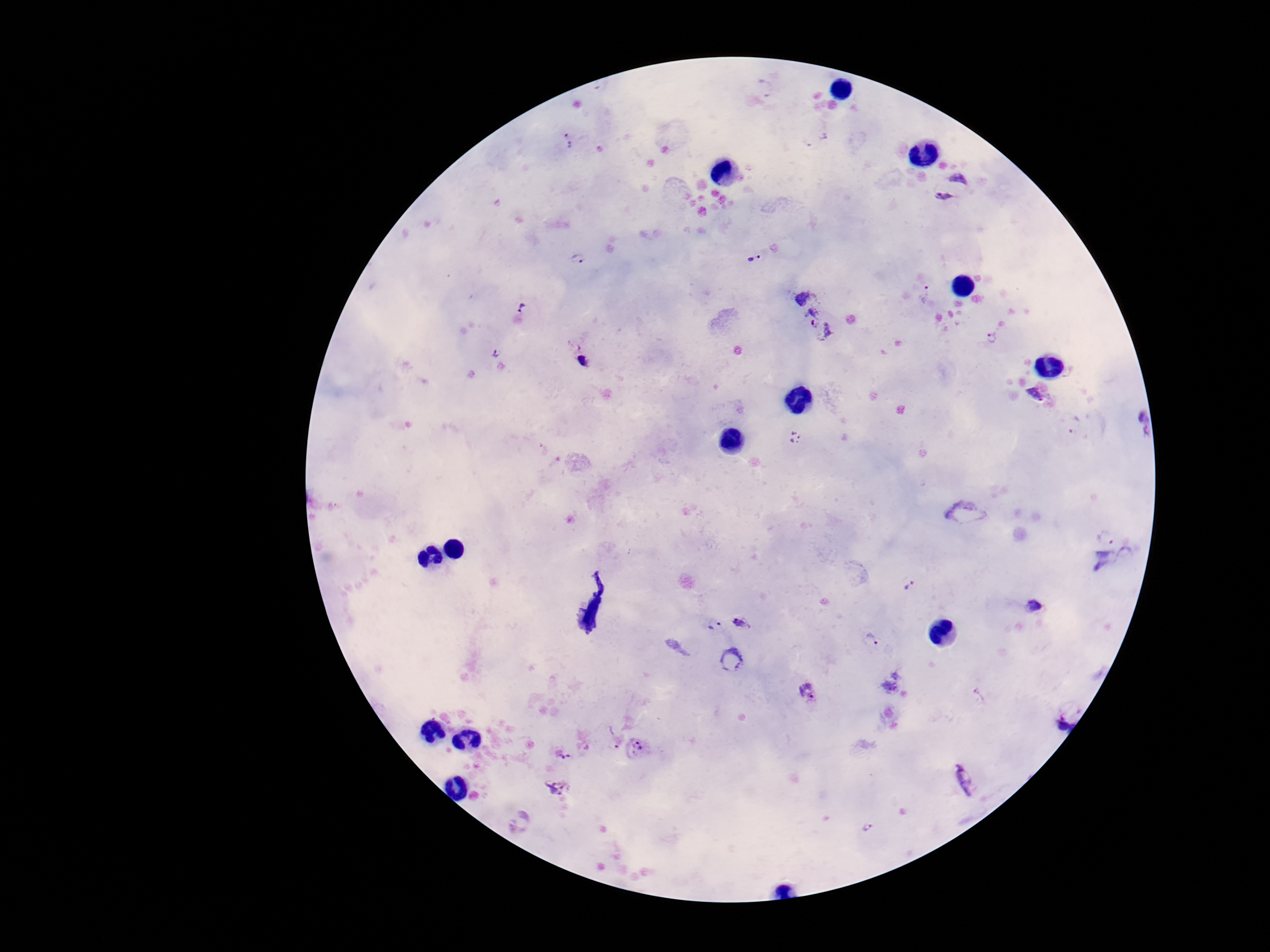

Approximate centers as [x, y] in pixels. Plasmodium parasite locations: [569, 141], [953, 189], [577, 258], [753, 261], [924, 294], [523, 305], [819, 323], [991, 337], [497, 351], [581, 359], [1035, 395], [1136, 422], [1075, 427], [797, 439], [966, 514], [1106, 536], [1128, 556], [1102, 562], [915, 588], [1034, 607], [741, 622], [713, 624], [872, 641], [731, 659], [809, 693], [1061, 720], [614, 736], [638, 747], [562, 751], [965, 780], [558, 789], [867, 828]. Giemsa-stained preparation. 100x magnification. Image is 1270×952 pixels. Thick blood smear. Photographed through the microscope eyepiece with a smartphone camera. Single field of view. Patient malaria status: infected.